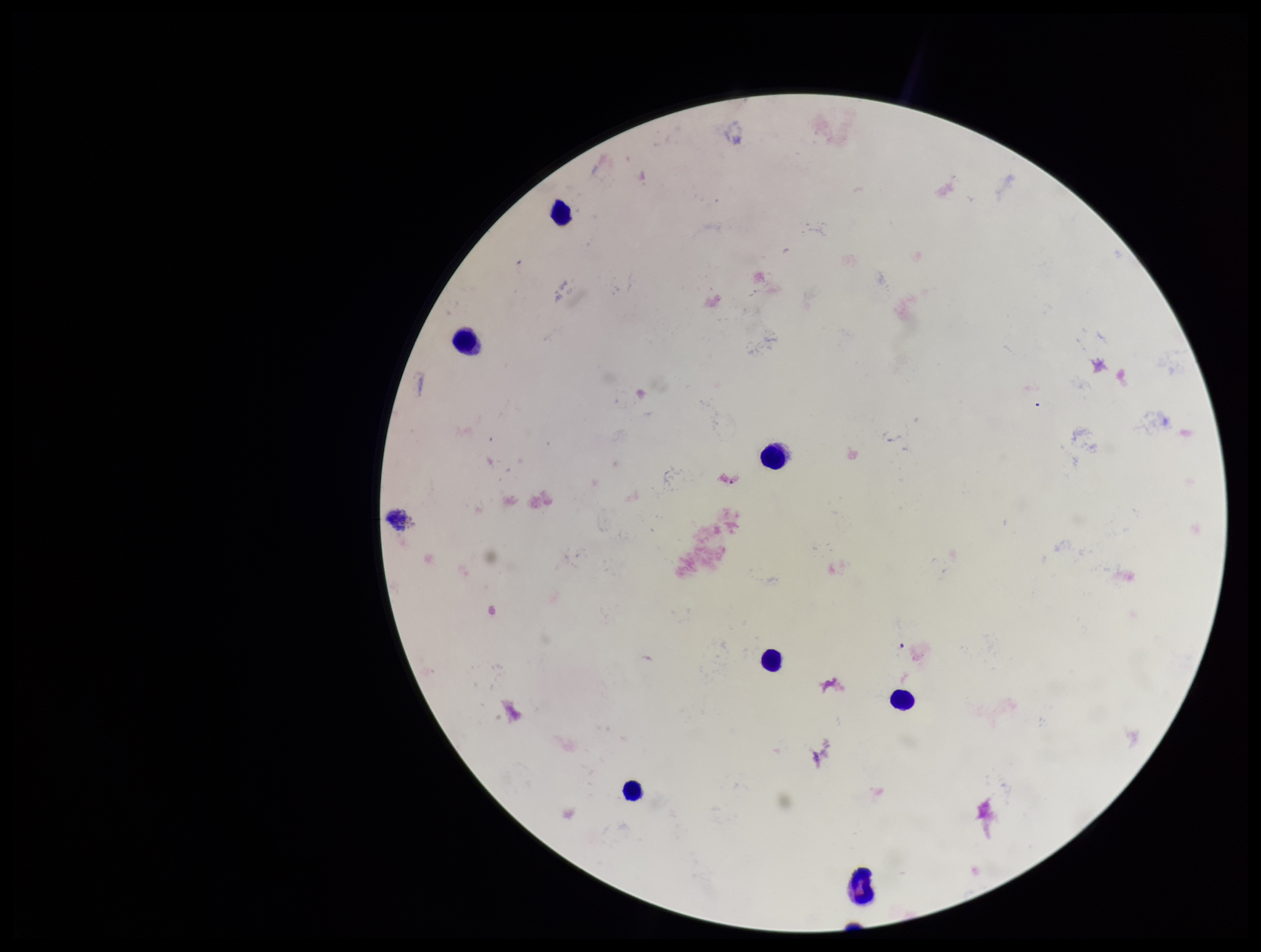

Summary:
  - Capture: smartphone photograph through the microscope eyepiece
  - Parasite count: 0
  - Stain: Giemsa
  - Preparation: thick smear
  - Image size: 1261×952 pixels
  - Patient malaria status: negative
  - Leukocyte count: 8
  - Field of view: one from this slide
  - Plasmodium parasites: none seen